Identify the parasite.
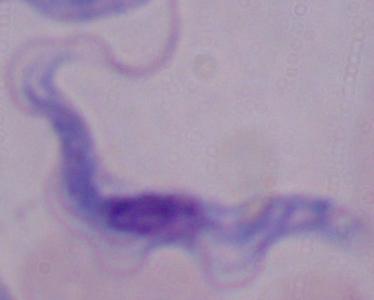
This is a trypanosome.

magnification = 1000x
modality = micrograph